Give the extent of all uninfected red blood cells.
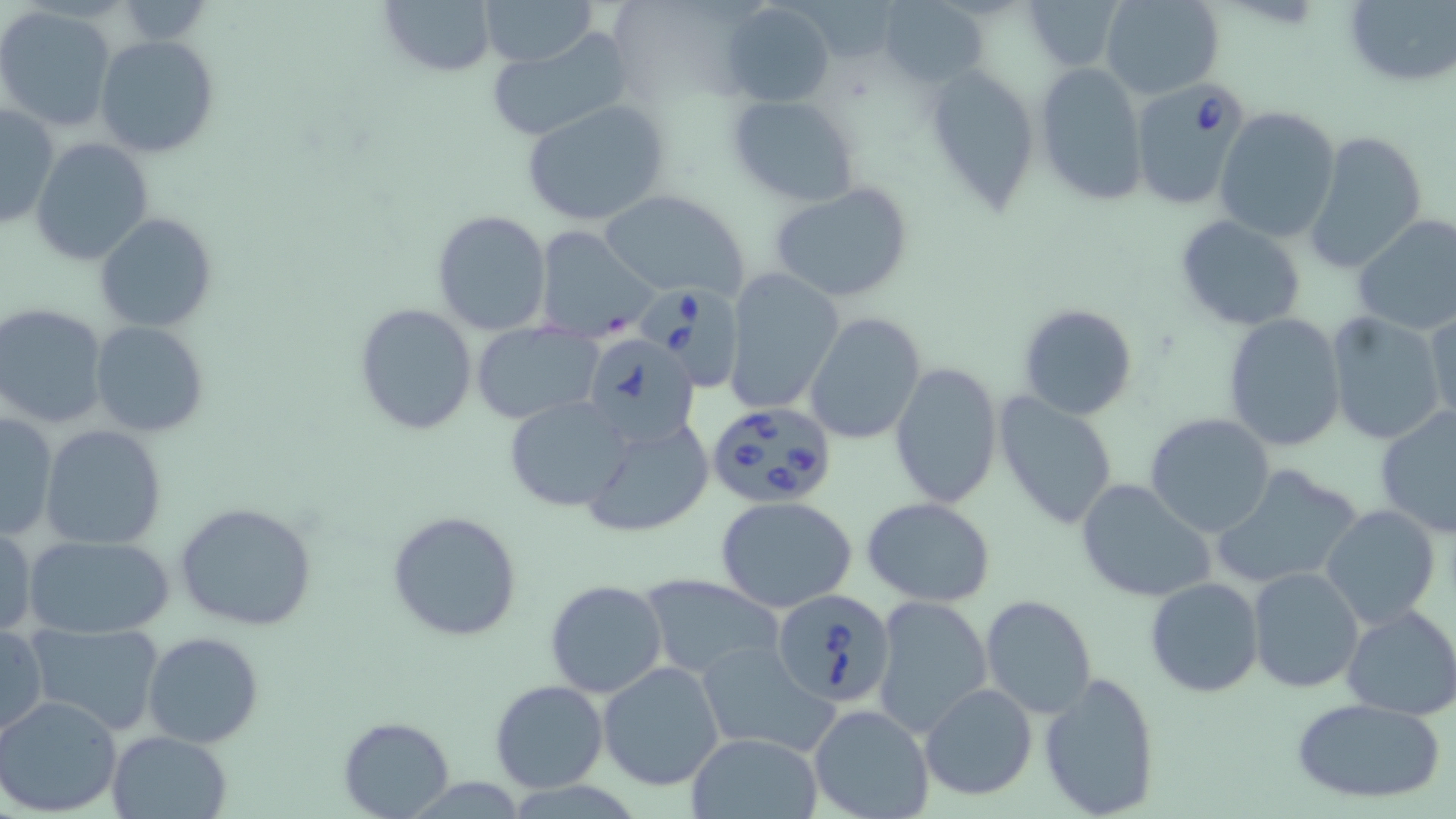
Approximate bounding boxes as (x1,y1)-(x2,y2) corner pairs in pixels.
Uninfected red blood cells: (375,0)-(497,75), (479,0)-(598,67), (1018,0)-(1124,72), (1098,0)-(1223,100), (1339,0)-(1456,88), (720,1)-(835,107), (769,1)-(901,63), (877,2)-(987,90), (0,7)-(118,133), (482,29)-(636,144), (94,34)-(220,157), (1033,59)-(1148,205), (922,60)-(1042,214), (727,95)-(860,207), (521,99)-(671,229), (1,101)-(58,230), (1214,105)-(1343,242), (1304,130)-(1429,274), (31,137)-(156,266), (768,181)-(917,304), (600,190)-(750,301), (431,209)-(553,337), (95,212)-(218,333), (1352,214)-(1456,338), (1175,215)-(1308,332), (534,226)-(656,340), (723,269)-(843,416), (353,302)-(479,437), (1,303)-(109,429), (1017,303)-(1139,422), (1426,304)-(1456,424), (804,312)-(927,446), (1222,312)-(1347,452), (1324,313)-(1447,446), (90,321)-(209,438), (468,323)-(600,424), (889,361)-(1002,510), (992,391)-(1120,531), (503,396)-(634,512), (1376,405)-(1456,538), (0,412)-(58,539), (1144,412)-(1277,538), (581,416)-(715,538), (40,424)-(167,550), (1216,466)-(1363,593), (1074,479)-(1216,603), (715,496)-(859,612), (864,497)-(996,605), (174,500)-(317,631), (1319,505)-(1441,630), (387,509)-(523,642), (0,523)-(37,639), (24,534)-(174,639), (1246,566)-(1365,695), (639,574)-(785,680), (1144,577)-(1264,698), (545,579)-(667,698), (980,595)-(1099,720), (872,596)-(993,736), (1341,604)-(1456,719), (27,621)-(167,738), (0,624)-(48,740), (142,632)-(266,748), (696,641)-(834,757), (598,660)-(725,791), (1038,670)-(1162,819), (488,680)-(609,794), (919,682)-(1040,802), (0,693)-(125,815), (1291,697)-(1446,804), (808,703)-(934,819), (337,716)-(454,818), (107,730)-(230,818), (686,732)-(822,818).

{
  "slide_level_diagnosis": "Babesia divergens",
  "modality": "optical microscopy",
  "preparation": "thin blood smear",
  "field_of_view": "one of a larger specimen",
  "babesia_divergens_infected_red_blood_cell_locations": "approximate bounding boxes as (x1,y1)-(x2,y2) corner pairs in pixels: (1131,79)-(1252,210), (640,280)-(747,391), (584,335)-(701,448), (706,400)-(840,512), (771,589)-(897,707)",
  "image_size": "1456×819 pixels",
  "magnification": "1000x",
  "stain": "May-Grünwald-Giemsa"
}